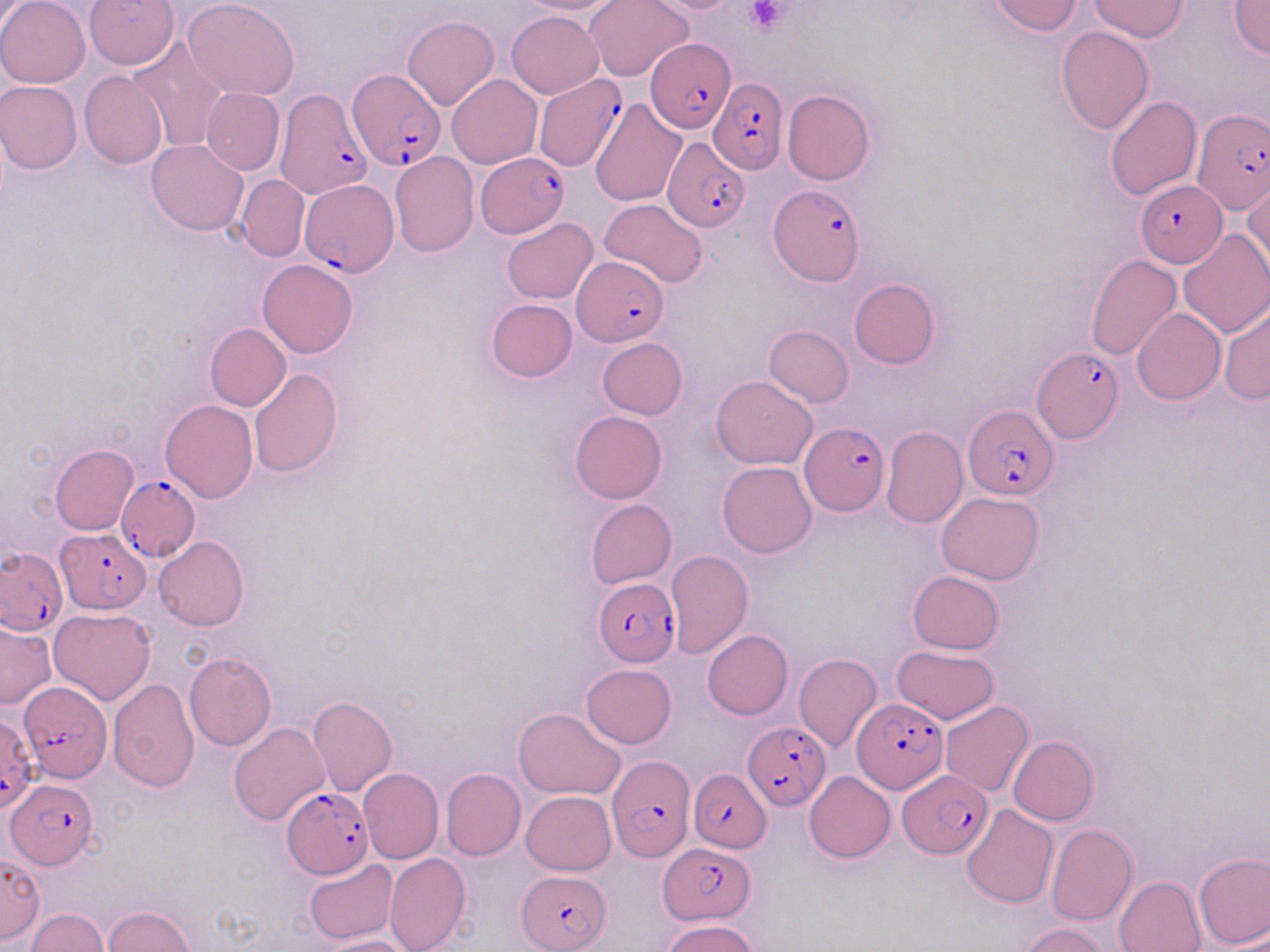
Approximate bounding boxes as [x1, y1, x2, y2] in pixels. Platelet locations: [744, 1, 792, 35]. Uninfected red blood cell locations: [0, 0, 90, 88], [85, 0, 178, 70], [183, 0, 299, 100], [515, 0, 631, 16], [585, 0, 693, 83], [642, 0, 745, 14], [987, 0, 1085, 35], [1089, 0, 1185, 41], [1228, 1, 1270, 60], [0, 3, 36, 43], [506, 11, 604, 98], [403, 15, 499, 110], [1056, 27, 1154, 135], [127, 38, 230, 152], [79, 72, 168, 170], [447, 74, 542, 168], [0, 81, 81, 174], [201, 87, 284, 175], [783, 90, 875, 186], [1106, 96, 1202, 200], [589, 98, 686, 207], [145, 139, 248, 235], [390, 152, 478, 258], [236, 174, 310, 261], [1243, 179, 1270, 279], [600, 197, 709, 287], [502, 216, 597, 304], [1179, 230, 1270, 338], [1086, 254, 1181, 361], [258, 259, 358, 359], [848, 278, 939, 368], [486, 299, 577, 382], [1219, 302, 1270, 404], [1132, 307, 1225, 405], [206, 323, 290, 411], [764, 325, 854, 406], [596, 337, 687, 419], [249, 368, 342, 478], [710, 375, 819, 469], [160, 400, 257, 501], [569, 410, 667, 503], [881, 426, 967, 530], [50, 444, 138, 534], [718, 461, 817, 558], [936, 492, 1045, 584], [585, 498, 676, 588], [153, 536, 250, 631], [665, 550, 752, 659], [907, 570, 1004, 654], [49, 607, 156, 705], [0, 621, 55, 710], [703, 630, 793, 719], [891, 646, 1000, 725], [184, 652, 277, 752], [793, 653, 882, 753], [580, 663, 677, 748], [106, 678, 199, 792], [307, 695, 396, 796], [940, 700, 1033, 797], [513, 708, 624, 799], [229, 721, 329, 825], [1008, 736, 1097, 825], [358, 768, 444, 863], [441, 769, 525, 859], [804, 771, 895, 863], [521, 790, 616, 876], [961, 803, 1058, 907], [1046, 825, 1138, 926], [1192, 851, 1270, 948], [384, 852, 471, 952], [0, 854, 44, 945], [304, 858, 398, 944], [1113, 875, 1207, 952], [104, 905, 194, 952], [26, 908, 109, 951], [662, 917, 760, 952], [1019, 923, 1110, 952], [322, 936, 416, 952]. Plasmodium falciparum-infected red blood cell locations: [645, 39, 739, 134], [348, 70, 448, 173], [537, 74, 627, 172], [708, 77, 787, 176], [274, 86, 372, 201], [1192, 110, 1269, 214], [661, 134, 747, 231], [476, 151, 568, 241], [299, 180, 398, 276], [1136, 180, 1225, 269], [769, 185, 864, 285], [572, 256, 669, 346], [1032, 349, 1123, 445], [961, 407, 1057, 499], [800, 422, 889, 514], [115, 474, 201, 562], [56, 529, 152, 613], [1, 545, 66, 635], [594, 577, 679, 666], [19, 681, 113, 783], [851, 697, 947, 796], [1, 710, 36, 810], [743, 722, 832, 810], [607, 753, 697, 861], [688, 769, 771, 852], [901, 772, 990, 857], [5, 776, 97, 868], [279, 788, 374, 878], [658, 842, 754, 923], [518, 869, 613, 951]. Slide-level diagnosis: Plasmodium falciparum. 1000x magnification. Single field of view. Image is 1270×952 pixels. Thin blood smear. Optical microscopy. May-Grünwald-Giemsa stain.